Report the malaria status of this cell.
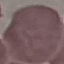
It is uninfected.

Summary:
  - Preparation: thin blood smear
  - Image type: automatically extracted cell patch, resized to 64 × 64 pixels
  - Stain: Giemsa
  - Capture: smartphone through the microscope eyepiece